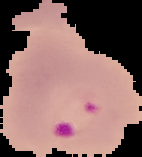
result = Plasmodium parasites identified
image size = 142×157 pixels
preparation = thin blood smear
image type = segmented cell region with the area outside set to black